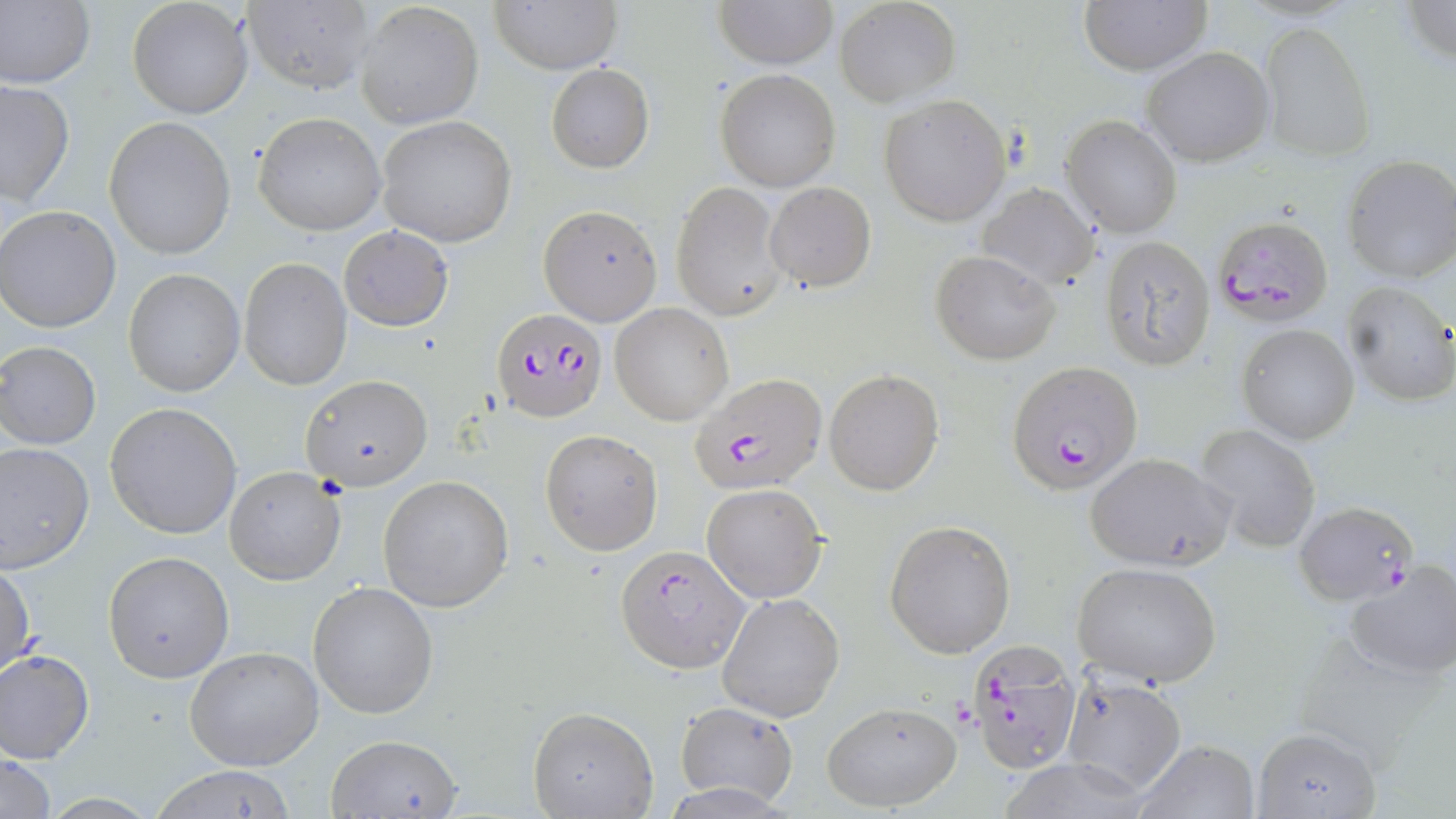 Approximate bounding boxes as (x1,y1)-(x2,y2) corner pairs in pixels. Uninfected red blood cell locations: (0,0)-(94,90), (127,0)-(253,120), (713,0)-(837,70), (1079,0)-(1213,73), (491,1)-(622,73), (834,1)-(960,108), (1404,1)-(1454,64), (242,2)-(373,92), (355,2)-(484,129), (1260,22)-(1373,161), (1142,46)-(1275,166), (546,63)-(654,172), (714,68)-(841,192), (1,79)-(75,207), (880,94)-(1011,226), (251,112)-(385,236), (104,115)-(236,260), (376,115)-(518,246), (1061,115)-(1184,239), (1341,154)-(1456,285), (671,180)-(787,321), (764,182)-(877,292), (975,182)-(1098,290), (540,204)-(663,324), (0,205)-(121,332), (339,225)-(453,331), (1098,235)-(1216,369), (931,249)-(1060,365), (239,256)-(352,392), (124,268)-(245,396), (1343,282)-(1456,407), (610,303)-(735,426), (1237,322)-(1360,446), (1,342)-(101,450), (823,369)-(944,495), (301,375)-(432,491), (105,402)-(243,540), (1196,423)-(1321,553), (540,429)-(663,555), (0,441)-(96,573), (1083,452)-(1234,572), (223,465)-(348,586), (378,474)-(514,612), (702,483)-(827,603), (884,520)-(1016,658), (103,550)-(236,683), (1343,559)-(1456,682), (1,560)-(36,680), (1071,561)-(1223,688), (308,583)-(438,720), (716,592)-(845,722), (1295,632)-(1441,763), (185,645)-(325,772), (0,649)-(95,764), (1059,672)-(1187,794), (672,700)-(799,804), (822,701)-(961,811), (527,705)-(658,819), (1251,727)-(1382,819), (323,734)-(466,818), (1131,739)-(1262,819), (0,752)-(57,819), (997,759)-(1155,819), (145,764)-(301,819). Plasmodium falciparum-infected red blood cell locations: (1217,219)-(1327,329), (491,307)-(608,422), (1008,363)-(1143,495), (687,374)-(826,494), (1293,502)-(1418,605), (616,546)-(748,674), (967,640)-(1081,774). Slide-level diagnosis: Plasmodium falciparum. 1000x magnification. Optical microscopy. Thin blood smear. Single field of view. May-Grünwald-Giemsa-stained preparation. Image is 1456×819 pixels.